Point out malaria parasites and leukocytes.
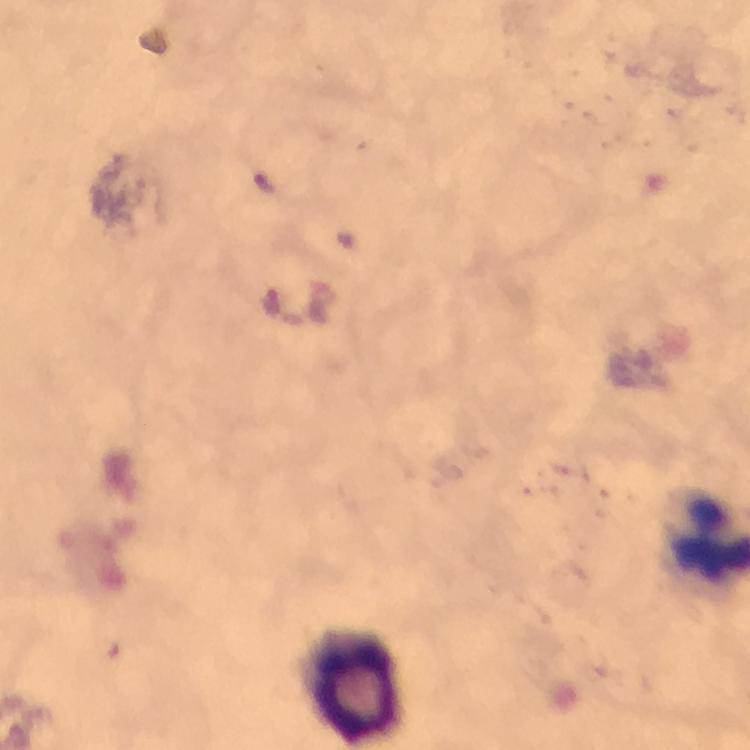
No malaria parasites detected.
Approximate centers as [x, y] in pixels.
Leukocytes: [354, 686].

Summary:
  - Image size: 750×750 pixels
  - Magnification: 100x
  - Context: from a malaria diagnostic workup
  - Immersion oil: used
  - Stain: Giemsa
  - Preparation: thick blood film
  - Capture: smartphone mounted on the microscope
  - Cropped from: one field of view